Assess the morphology of the erythrocytes.
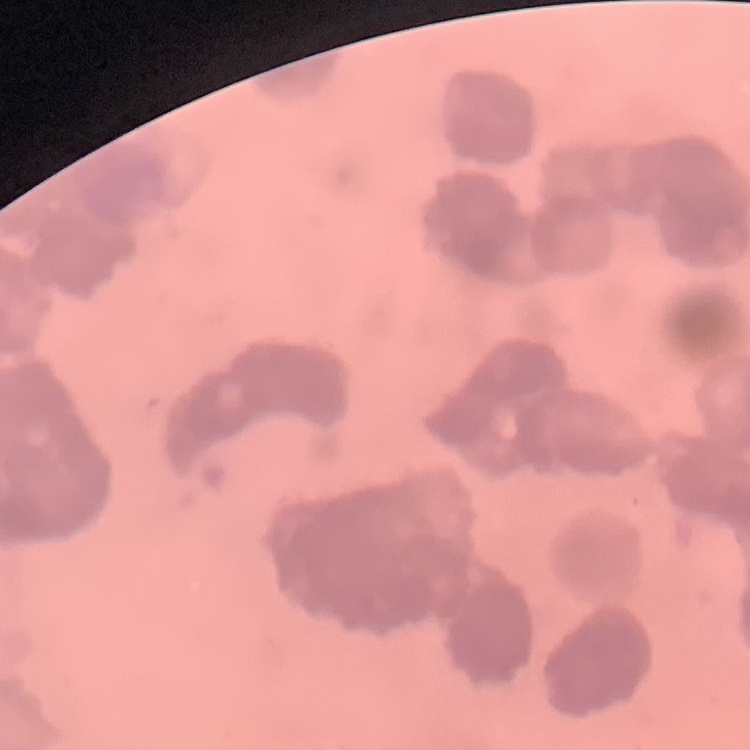

Rouleaux formation.

Square crop of a larger photomicrograph. Field's or Giemsa stain. Thin blood film.